Identify the cell.
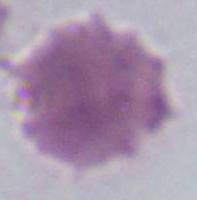
An erythrocyte.

magnification: 1000x
modality: photomicrograph